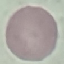

Summary:
  - Result: no malaria parasites seen
  - Preparation: thin smear
  - Image type: cell patch, automatically extracted from a larger field of view and resized to 64 × 64 pixels
  - Capture: smartphone through the microscope eyepiece
  - Stain: Giemsa